Report the malaria status of this cell.
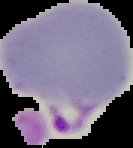

It is parasitized.

image size = 133×148 pixels
preparation = thin blood film
image type = segmented cell region on a black background